Report the malaria status of this cell.
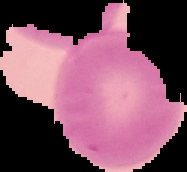

Uninfected.

preparation: thin blood smear
image_type: segmented cell region with the area outside set to black
image_size: 187×172 pixels